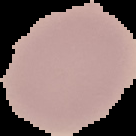

preparation: thin blood film
image_type: cell region segmented out of the field of view; surrounding area masked to black
image_size: 136×136 pixels
malaria_status: uninfected